Assess this cell for malaria.
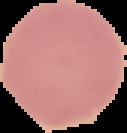
It is uninfected.

Summary:
  - Preparation: thin blood film
  - Image type: cell region segmented out of the field of view; surrounding area masked to black
  - Image size: 127×133 pixels